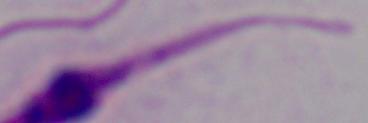

{
  "identification": "Leishmania",
  "magnification": "1000x",
  "modality": "micrograph"
}